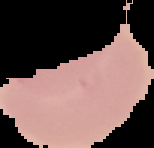

Summary:
  - Image type: cell region segmented out of the field of view; surrounding area masked to black
  - Preparation: thin blood smear
  - Image size: 154×148 pixels
  - Malaria status: uninfected